State the blood parasite species.
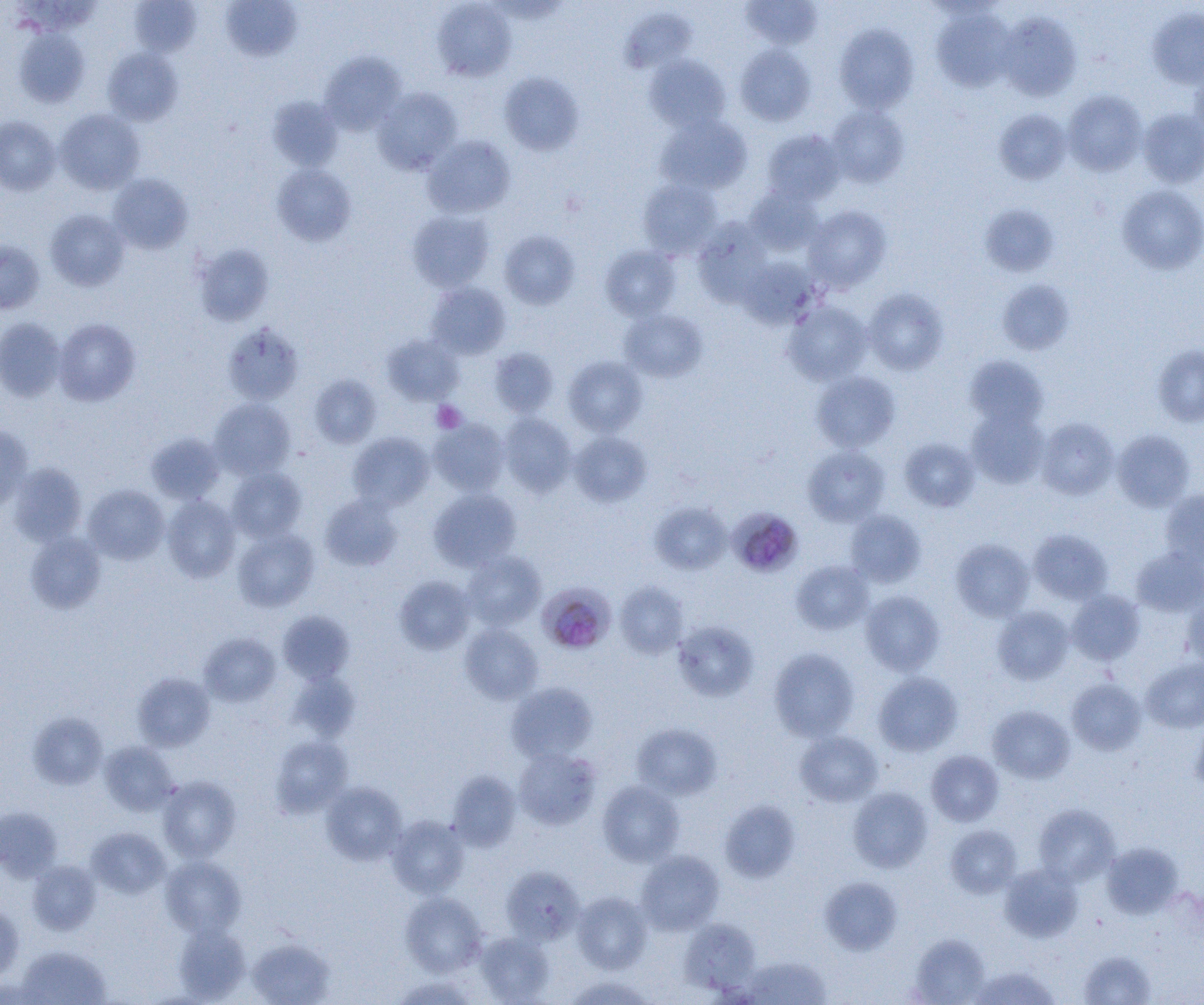

Plasmodium malariae.

Summary:
  - Coordinate format: approximate bounding boxes as (x1, y1, x2, y2) in pixels
  - Uninfected red blood cell locations: (742, 0, 822, 50), (130, 1, 201, 56), (220, 1, 303, 62), (432, 1, 516, 82), (932, 6, 1015, 93), (621, 7, 696, 74), (1148, 7, 1204, 90), (997, 12, 1082, 102), (834, 24, 918, 113), (14, 28, 89, 107), (734, 45, 816, 126), (103, 47, 183, 125), (320, 51, 405, 134), (644, 55, 731, 132), (1188, 62, 1204, 146), (499, 72, 583, 155), (373, 87, 462, 174), (1063, 89, 1147, 176), (268, 96, 343, 171), (826, 104, 909, 188), (994, 108, 1072, 184), (1137, 108, 1204, 188), (55, 109, 145, 194), (655, 115, 752, 195), (0, 116, 61, 195), (762, 129, 845, 205), (423, 135, 515, 218), (271, 164, 356, 246), (108, 173, 193, 254), (638, 178, 722, 259), (1117, 184, 1204, 274), (744, 186, 823, 255), (980, 203, 1059, 276), (803, 205, 892, 292), (45, 209, 129, 291), (407, 210, 495, 292), (694, 219, 771, 307), (499, 230, 579, 309), (0, 240, 45, 314), (193, 244, 274, 326), (600, 245, 681, 321), (739, 258, 821, 329), (996, 279, 1074, 354), (426, 282, 511, 359), (862, 288, 948, 375), (783, 302, 872, 386), (619, 309, 708, 382), (0, 317, 66, 402), (54, 318, 141, 406), (223, 323, 304, 405), (382, 334, 464, 405), (1152, 345, 1204, 427), (489, 348, 559, 417), (965, 355, 1048, 429), (563, 356, 647, 437), (811, 370, 900, 452), (309, 374, 382, 448), (209, 397, 296, 479), (967, 409, 1049, 488), (499, 412, 577, 497), (430, 418, 509, 496), (1036, 418, 1119, 500), (0, 425, 33, 511), (1112, 429, 1195, 511), (146, 432, 225, 504), (348, 432, 433, 510), (569, 432, 652, 507), (899, 438, 980, 512), (803, 445, 890, 526), (7, 462, 87, 547), (227, 466, 307, 542), (83, 484, 169, 564), (428, 488, 521, 572), (1160, 490, 1204, 569), (320, 493, 403, 571), (162, 495, 241, 582), (650, 502, 731, 574), (845, 510, 926, 588), (232, 528, 319, 612), (1028, 529, 1113, 605), (25, 531, 107, 613), (951, 539, 1034, 621), (1131, 547, 1204, 617), (462, 551, 546, 630), (791, 561, 873, 634), (394, 575, 475, 655), (615, 582, 688, 658), (1067, 589, 1145, 666), (860, 590, 944, 675), (1182, 590, 1204, 668), (992, 605, 1074, 685), (278, 611, 354, 683), (673, 620, 758, 702), (460, 623, 543, 704), (200, 632, 280, 706), (769, 648, 859, 741), (1140, 657, 1204, 733), (288, 671, 359, 741), (873, 671, 963, 756), (133, 672, 214, 751), (1066, 678, 1147, 755), (506, 682, 598, 763), (988, 705, 1075, 783), (28, 711, 107, 790), (1190, 716, 1204, 795), (631, 723, 722, 800), (795, 730, 883, 807), (270, 736, 352, 817), (100, 741, 178, 815), (514, 748, 601, 830), (926, 750, 1003, 826), (447, 770, 521, 851), (157, 775, 241, 862), (598, 780, 685, 866), (321, 782, 407, 865), (847, 786, 932, 872), (719, 799, 801, 883), (1033, 803, 1120, 886), (0, 806, 62, 882), (387, 815, 469, 898), (946, 825, 1022, 898), (86, 827, 171, 898), (1101, 842, 1183, 918), (635, 850, 724, 935), (161, 856, 246, 937), (27, 860, 101, 935), (999, 863, 1083, 942), (501, 866, 584, 945), (819, 876, 902, 954), (400, 891, 487, 976), (571, 891, 653, 974), (0, 903, 23, 981), (679, 919, 760, 995), (174, 924, 250, 1002), (475, 932, 554, 1004), (910, 934, 990, 1005), (247, 937, 335, 1005), (16, 945, 111, 1004), (1078, 950, 1157, 1005), (740, 955, 832, 1004), (970, 965, 1060, 1005), (390, 975, 480, 1004), (562, 975, 658, 1005)
  - Plasmodium malariae-infected red blood cell locations: (729, 508, 802, 578), (542, 582, 619, 655)
  - Platelet locations: (432, 401, 466, 433)
  - Image size: 1204×1005 pixels
  - Preparation: thin blood film
  - Magnification: 1000x
  - Modality: optical microscopy
  - Field of view: one of a larger specimen